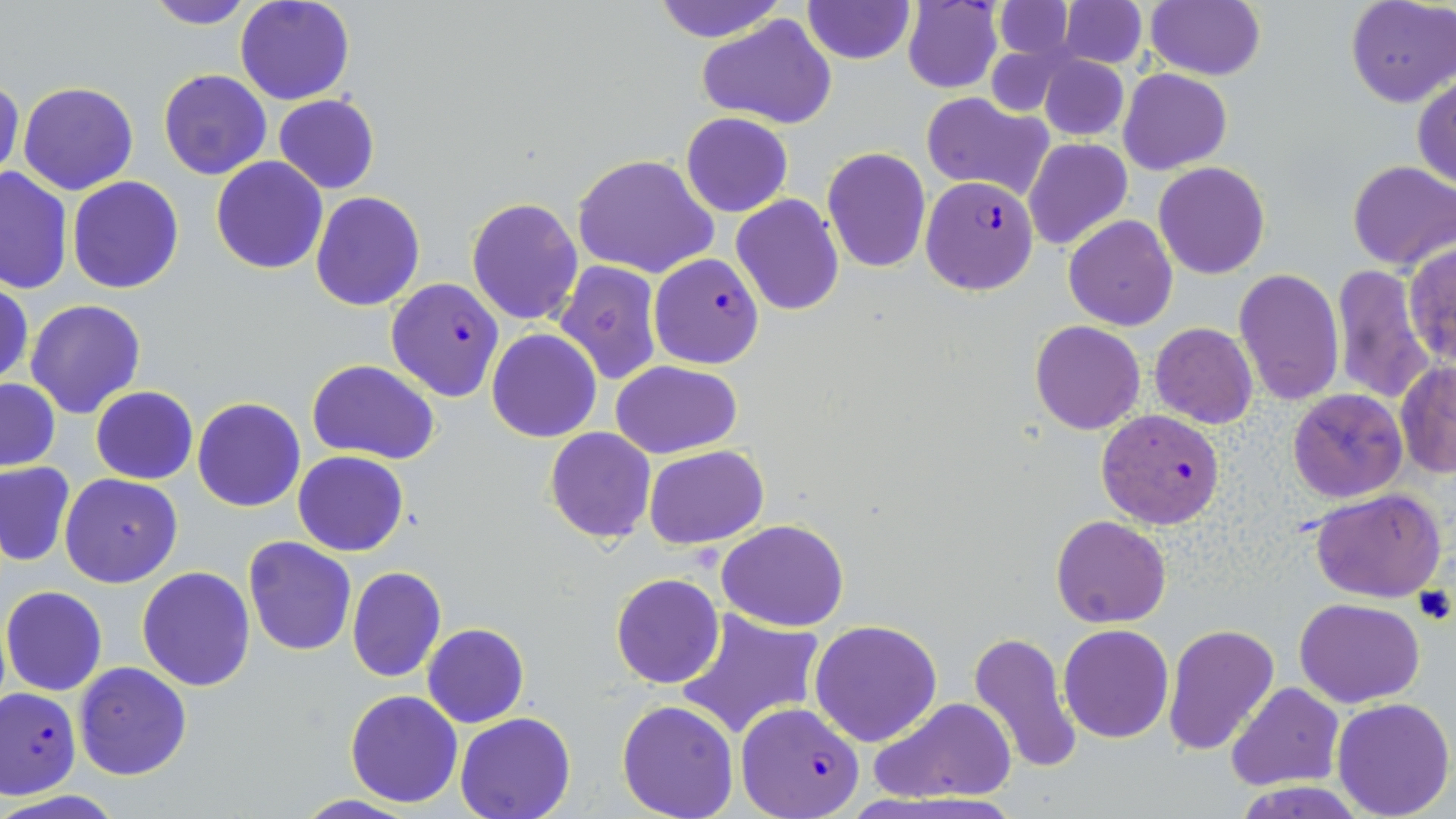

Approximate bounding boxes as named x1/y1/x2/y2 corners in pixels. Uninfected red blood cell locations: (x1=143, y1=0, x2=257, y2=28), (x1=236, y1=0, x2=354, y2=105), (x1=648, y1=0, x2=786, y2=42), (x1=804, y1=0, x2=912, y2=64), (x1=1146, y1=0, x2=1265, y2=81), (x1=1346, y1=0, x2=1455, y2=107), (x1=903, y1=1, x2=1003, y2=93), (x1=992, y1=1, x2=1076, y2=62), (x1=1058, y1=1, x2=1146, y2=69), (x1=697, y1=13, x2=837, y2=129), (x1=1036, y1=52, x2=1130, y2=141), (x1=157, y1=68, x2=272, y2=180), (x1=1119, y1=68, x2=1232, y2=174), (x1=1412, y1=76, x2=1456, y2=189), (x1=0, y1=78, x2=24, y2=185), (x1=19, y1=81, x2=137, y2=195), (x1=923, y1=93, x2=1053, y2=199), (x1=273, y1=94, x2=379, y2=194), (x1=682, y1=112, x2=791, y2=217), (x1=1025, y1=138, x2=1132, y2=250), (x1=822, y1=147, x2=932, y2=272), (x1=1040, y1=147, x2=1153, y2=319), (x1=572, y1=155, x2=717, y2=277), (x1=211, y1=156, x2=327, y2=274), (x1=1347, y1=159, x2=1456, y2=270), (x1=1154, y1=162, x2=1269, y2=279), (x1=1, y1=166, x2=73, y2=295), (x1=67, y1=175, x2=186, y2=294), (x1=311, y1=191, x2=425, y2=311), (x1=732, y1=195, x2=844, y2=315), (x1=467, y1=199, x2=582, y2=326), (x1=1064, y1=215, x2=1179, y2=330), (x1=1404, y1=245, x2=1456, y2=368), (x1=554, y1=260, x2=663, y2=385), (x1=1331, y1=262, x2=1433, y2=403), (x1=1233, y1=268, x2=1344, y2=405), (x1=0, y1=277, x2=33, y2=390), (x1=24, y1=299, x2=147, y2=419), (x1=1030, y1=321, x2=1145, y2=435), (x1=1150, y1=323, x2=1258, y2=429), (x1=487, y1=329, x2=600, y2=442), (x1=308, y1=360, x2=440, y2=464), (x1=610, y1=360, x2=742, y2=458), (x1=1394, y1=362, x2=1456, y2=478), (x1=0, y1=378, x2=60, y2=471), (x1=90, y1=386, x2=197, y2=484), (x1=1287, y1=388, x2=1407, y2=502), (x1=192, y1=397, x2=305, y2=511), (x1=544, y1=427, x2=656, y2=543), (x1=644, y1=446, x2=768, y2=547), (x1=293, y1=450, x2=409, y2=557), (x1=0, y1=462, x2=75, y2=566), (x1=60, y1=473, x2=182, y2=587), (x1=1310, y1=490, x2=1446, y2=603), (x1=1051, y1=514, x2=1172, y2=628), (x1=717, y1=518, x2=850, y2=632), (x1=243, y1=537, x2=357, y2=657), (x1=135, y1=566, x2=256, y2=692), (x1=346, y1=567, x2=446, y2=682), (x1=610, y1=573, x2=724, y2=689), (x1=2, y1=585, x2=107, y2=696), (x1=1295, y1=598, x2=1425, y2=707), (x1=675, y1=608, x2=825, y2=743), (x1=810, y1=619, x2=942, y2=747), (x1=1059, y1=623, x2=1174, y2=743), (x1=423, y1=624, x2=529, y2=728), (x1=1162, y1=624, x2=1280, y2=757), (x1=967, y1=632, x2=1083, y2=776), (x1=73, y1=661, x2=193, y2=781), (x1=1226, y1=682, x2=1344, y2=789), (x1=345, y1=690, x2=463, y2=807), (x1=868, y1=695, x2=1018, y2=805), (x1=1331, y1=698, x2=1455, y2=818), (x1=616, y1=699, x2=739, y2=819), (x1=455, y1=711, x2=577, y2=819), (x1=0, y1=791, x2=129, y2=819), (x1=293, y1=795, x2=420, y2=818). Plasmodium falciparum-infected red blood cell locations: (x1=921, y1=175, x2=1040, y2=295), (x1=649, y1=254, x2=764, y2=369), (x1=386, y1=278, x2=503, y2=401), (x1=1097, y1=407, x2=1223, y2=530), (x1=1, y1=685, x2=80, y2=799), (x1=735, y1=702, x2=865, y2=819). Slide-level diagnosis: Plasmodium falciparum. Optical microscopy. Image is 1456×819 pixels. One field of a larger specimen. May-Grünwald-Giemsa-stained preparation. Captured at 1000x magnification. Thin blood smear.